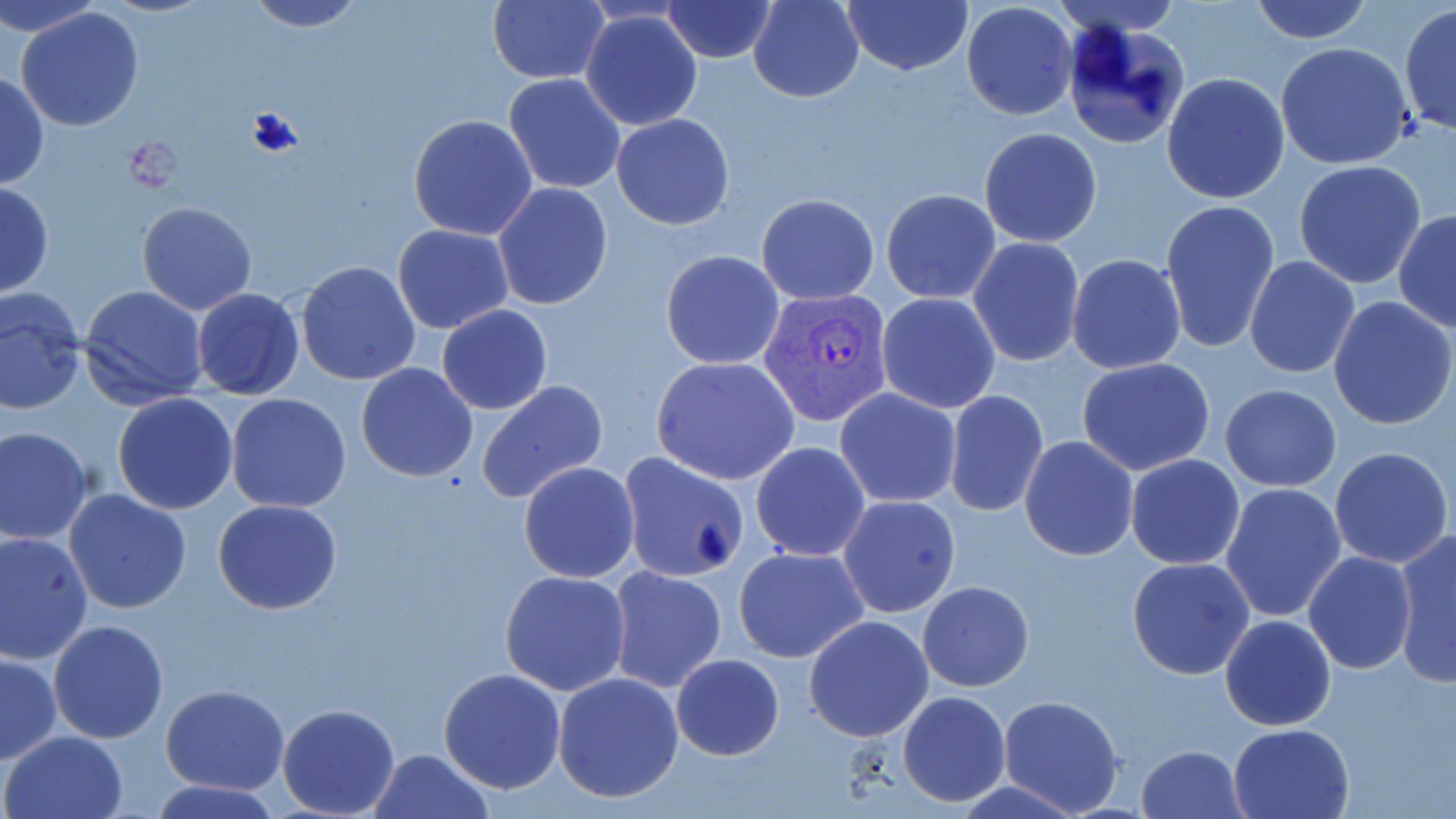
slide_level_diagnosis: Plasmodium vivax
field_of_view: one of a larger specimen
image_size: 1456×819 pixels
stain: May-Grünwald-Giemsa
uninfected_red_blood_cell_locations: 'approximate bounding boxes as (x1, y1, x2, y2) in pixels: (0, 0, 109, 38), (240, 0, 367, 32), (487, 0, 609, 86), (662, 0, 776, 64), (749, 0, 864, 102), (842, 0, 972, 74), (1051, 0, 1186, 39), (1245, 0, 1375, 45), (960, 1, 1079, 120), (1399, 3, 1456, 141), (13, 7, 145, 131), (580, 9, 704, 130), (1059, 20, 1189, 151), (1276, 42, 1416, 171), (0, 71, 48, 190), (504, 73, 625, 195), (1162, 73, 1290, 205), (612, 112, 735, 231), (408, 114, 538, 240), (978, 128, 1103, 247), (1294, 160, 1427, 288), (0, 181, 53, 297), (492, 183, 613, 312), (880, 189, 1002, 305), (756, 194, 879, 305), (1160, 200, 1280, 351), (136, 202, 257, 315), (1393, 211, 1456, 332), (391, 223, 515, 334), (968, 237, 1086, 368), (660, 251, 785, 369), (1065, 254, 1186, 376), (1245, 256, 1360, 377), (295, 261, 421, 386), (78, 285, 209, 410), (1, 288, 85, 416), (191, 288, 306, 401), (876, 293, 1002, 412), (1328, 296, 1455, 431), (436, 305, 554, 415), (651, 356, 801, 486), (1077, 358, 1216, 475), (355, 363, 479, 482), (477, 379, 608, 506), (1221, 383, 1341, 491), (835, 387, 961, 507), (944, 391, 1048, 515), (112, 393, 239, 514), (224, 393, 352, 513), (0, 426, 93, 544), (1019, 437, 1139, 559), (750, 441, 871, 562), (1329, 446, 1452, 569), (617, 450, 750, 581), (1125, 455, 1246, 569), (518, 462, 639, 583), (1221, 482, 1348, 621), (63, 487, 193, 614), (838, 494, 960, 618), (213, 499, 341, 615), (0, 530, 94, 663), (1394, 530, 1456, 684), (734, 545, 868, 663), (1303, 552, 1416, 675), (1126, 557, 1255, 679), (607, 565, 727, 693), (500, 569, 631, 695), (918, 580, 1033, 691), (1220, 614, 1336, 731), (804, 616, 933, 741), (48, 620, 169, 744), (1, 652, 61, 764), (670, 653, 785, 760), (439, 667, 566, 793), (552, 671, 684, 804), (161, 684, 291, 796), (897, 691, 1010, 807), (996, 694, 1125, 817), (276, 702, 401, 817), (1228, 723, 1355, 818), (1, 731, 128, 819), (1137, 742, 1249, 818), (367, 748, 494, 819), (153, 778, 281, 817)'
plasmodium_vivax_infected_red_blood_cell_locations: 'approximate bounding boxes as (x1, y1, x2, y2) in pixels: (759, 287, 895, 428)'
preparation: thin blood smear
magnification: 1000x
modality: light microscopy